Point out each leukocyte.
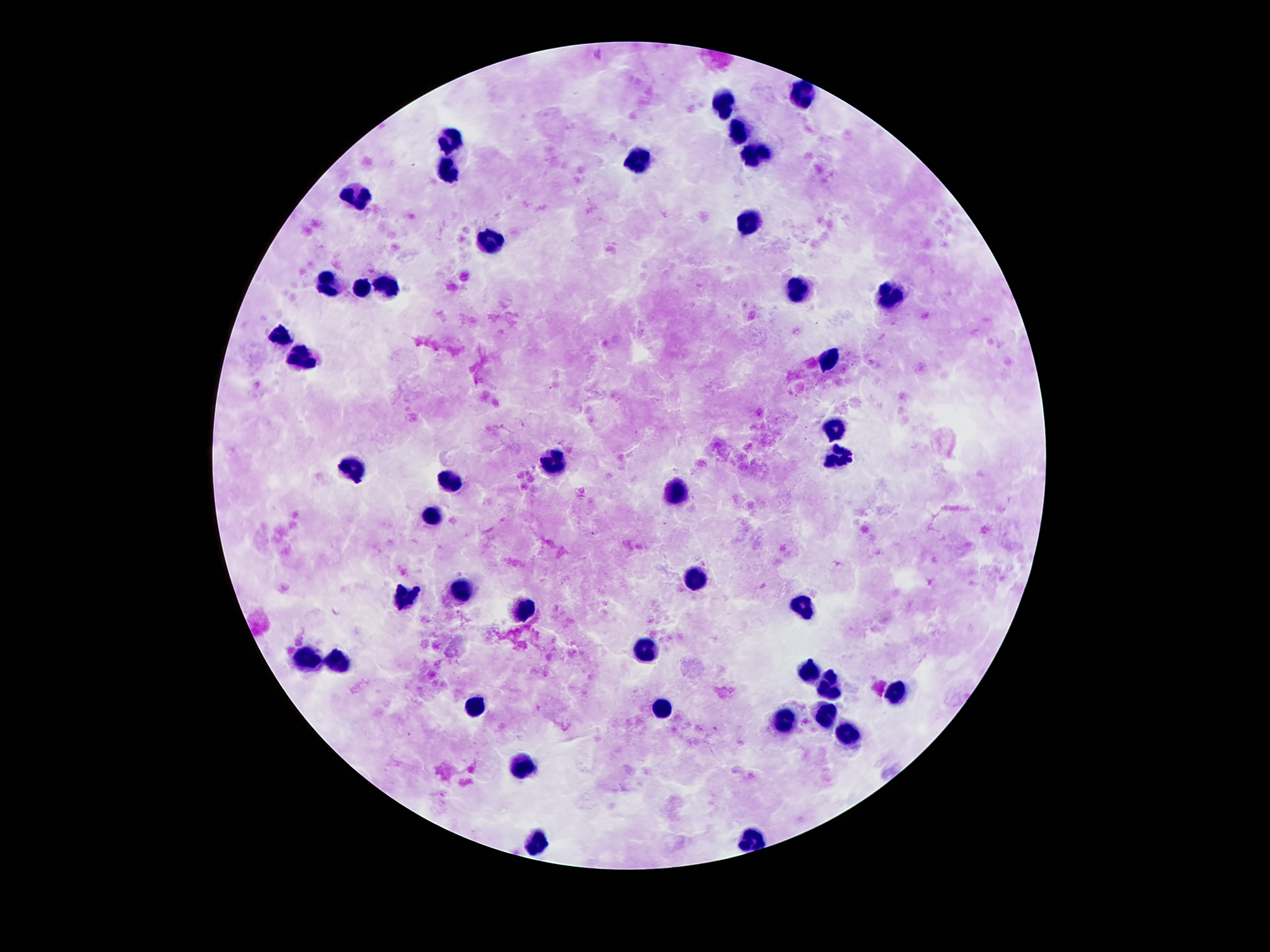
Approximate centers as [x, y] in pixels.
Leukocytes: [803, 94], [727, 100], [736, 128], [456, 137], [753, 148], [635, 165], [449, 169], [355, 197], [749, 219], [488, 243], [387, 279], [327, 283], [363, 286], [794, 288], [889, 296], [277, 339], [829, 359], [299, 363], [833, 426], [835, 458], [551, 462], [350, 469], [449, 479], [676, 494], [432, 518], [693, 574], [464, 585], [406, 596], [521, 608], [803, 608], [645, 652], [305, 658], [340, 660], [811, 669], [828, 688], [893, 692], [471, 701], [663, 707], [820, 718], [783, 723], [844, 735], [523, 761], [751, 837], [536, 841].

Single field of view. 100x magnification. Giemsa stain. Thick blood smear. Image is 1270×952 pixels. Patient malaria status: uninfected. Smartphone photograph taken through the microscope eyepiece.